Report the malaria status of this cell.
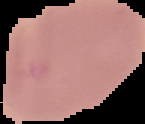
It is uninfected.

From a thin blood smear. Cell region segmented out of the field of view; the surrounding area is masked to black. Image is 145×124 pixels.